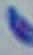

Summary:
  - Identification: Toxoplasma gondii
  - Magnification: 1000x
  - Modality: micrograph